Classify this cell by malaria status.
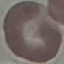
It is uninfected.

stain = Giemsa
image type = automatically extracted cell patch, resized to 64 × 64 pixels
capture = smartphone camera at the microscope eyepiece
preparation = thin blood smear